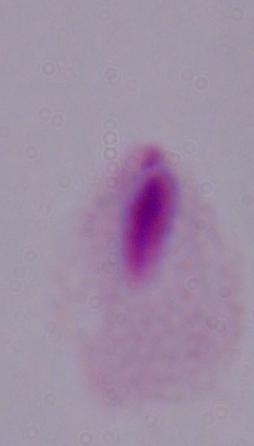
{
  "modality": "micrograph",
  "magnification": "1000x",
  "identification": "trichomonad"
}